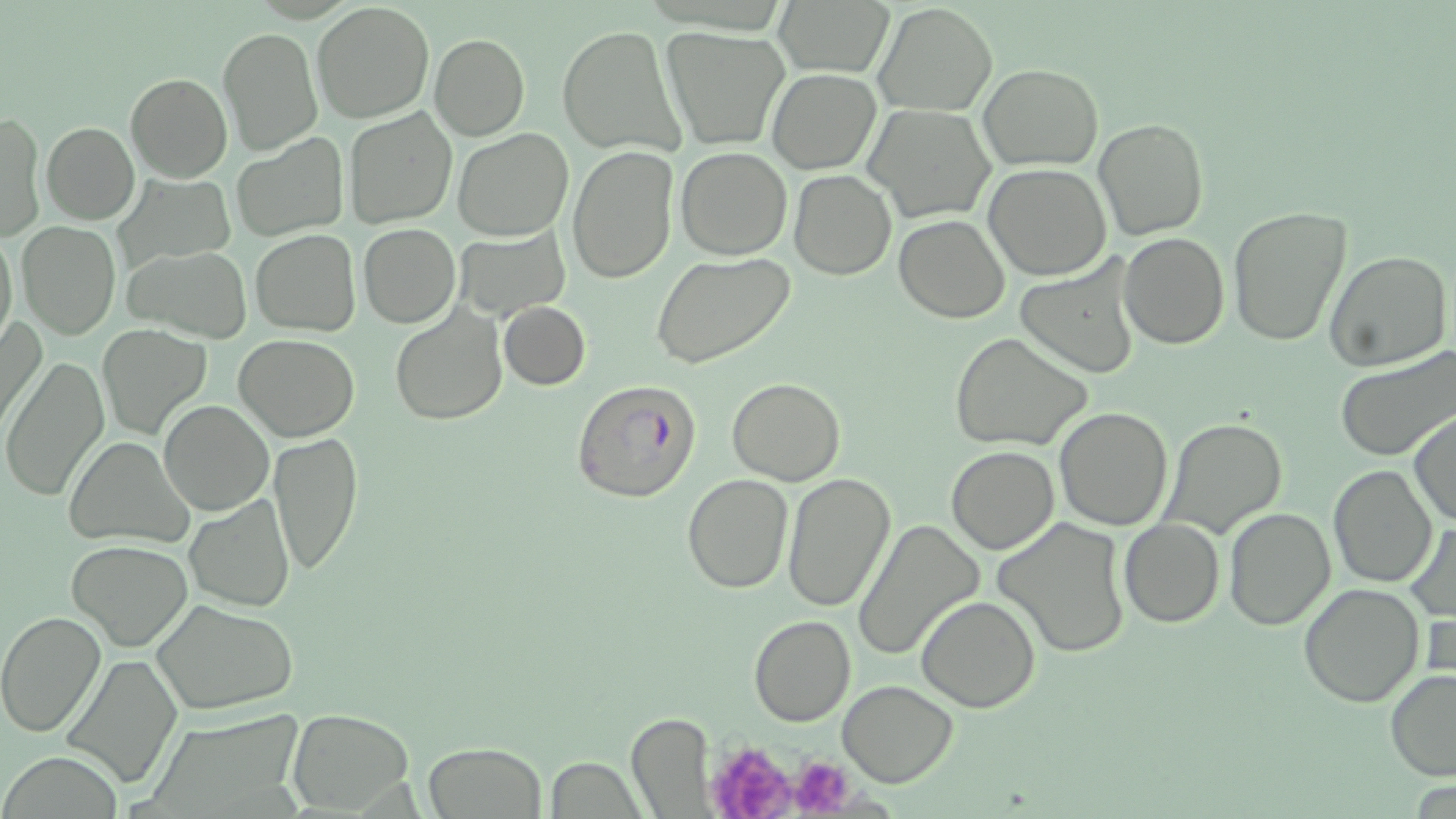
Summary:
  - Coordinate format: approximate bounding boxes as (x1, y1, x2, y2) in pixels
  - Plasmodium falciparum-infected red blood cell locations: (574, 380, 701, 503)
  - Uninfected red blood cell locations: (313, 2, 434, 121), (772, 2, 892, 76), (874, 2, 996, 116), (557, 24, 685, 158), (217, 25, 322, 156), (662, 27, 788, 150), (429, 34, 530, 140), (978, 64, 1103, 170), (768, 69, 879, 174), (125, 73, 232, 182), (866, 105, 993, 222), (343, 107, 457, 229), (1, 111, 43, 242), (1093, 119, 1210, 240), (42, 122, 140, 223), (451, 130, 574, 241), (230, 132, 346, 241), (568, 145, 679, 285), (675, 147, 793, 260), (984, 163, 1112, 280), (789, 169, 896, 279), (1227, 204, 1352, 347), (894, 215, 1009, 323), (17, 221, 121, 337), (358, 222, 459, 328), (0, 228, 18, 348), (249, 230, 360, 334), (455, 231, 570, 321), (1119, 232, 1228, 349), (483, 237, 581, 393), (125, 245, 253, 343), (1323, 248, 1452, 373), (652, 252, 796, 369), (1015, 257, 1142, 377), (499, 302, 590, 389), (390, 303, 507, 424), (1, 316, 45, 439), (97, 323, 211, 440), (950, 332, 1093, 451), (234, 334, 360, 440), (1334, 345, 1455, 461), (2, 357, 109, 502), (727, 377, 845, 485), (158, 401, 273, 516), (1054, 407, 1175, 529), (1410, 411, 1455, 527), (1161, 418, 1288, 539), (267, 430, 364, 578), (64, 436, 193, 550), (946, 446, 1059, 554), (1329, 464, 1436, 586), (782, 472, 896, 613), (683, 473, 792, 592), (185, 495, 295, 612), (1224, 505, 1336, 629), (852, 516, 985, 661), (992, 516, 1133, 660), (1118, 518, 1223, 627), (1407, 520, 1454, 621), (66, 539, 192, 650), (1299, 581, 1425, 706), (916, 594, 1039, 712), (153, 598, 297, 713), (0, 610, 106, 737), (749, 614, 856, 727), (60, 652, 181, 788), (1385, 667, 1456, 780), (836, 678, 959, 787), (162, 704, 316, 814), (289, 709, 414, 813), (626, 710, 713, 817), (423, 741, 547, 819), (547, 758, 647, 817)
  - Platelet locations: (716, 740, 796, 819), (781, 757, 856, 817)
  - Slide-level diagnosis: Plasmodium falciparum
  - Modality: optical microscopy
  - Field of view: one of a larger specimen
  - Preparation: thin blood film
  - Image size: 1456×819 pixels
  - Stain: May-Grünwald-Giemsa
  - Magnification: 1000x